Report the malaria status of this cell.
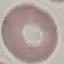
Uninfected.

Photographed with a smartphone camera at the microscope eyepiece. Thin blood film. Cell patch, automatically extracted from a larger field of view and resized to 64 × 64 pixels. Giemsa stain.